State which parasite is depicted.
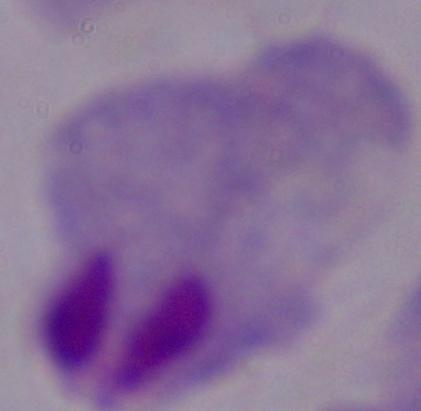

A trichomonad.

Captured at 1000x magnification. Photomicrograph.